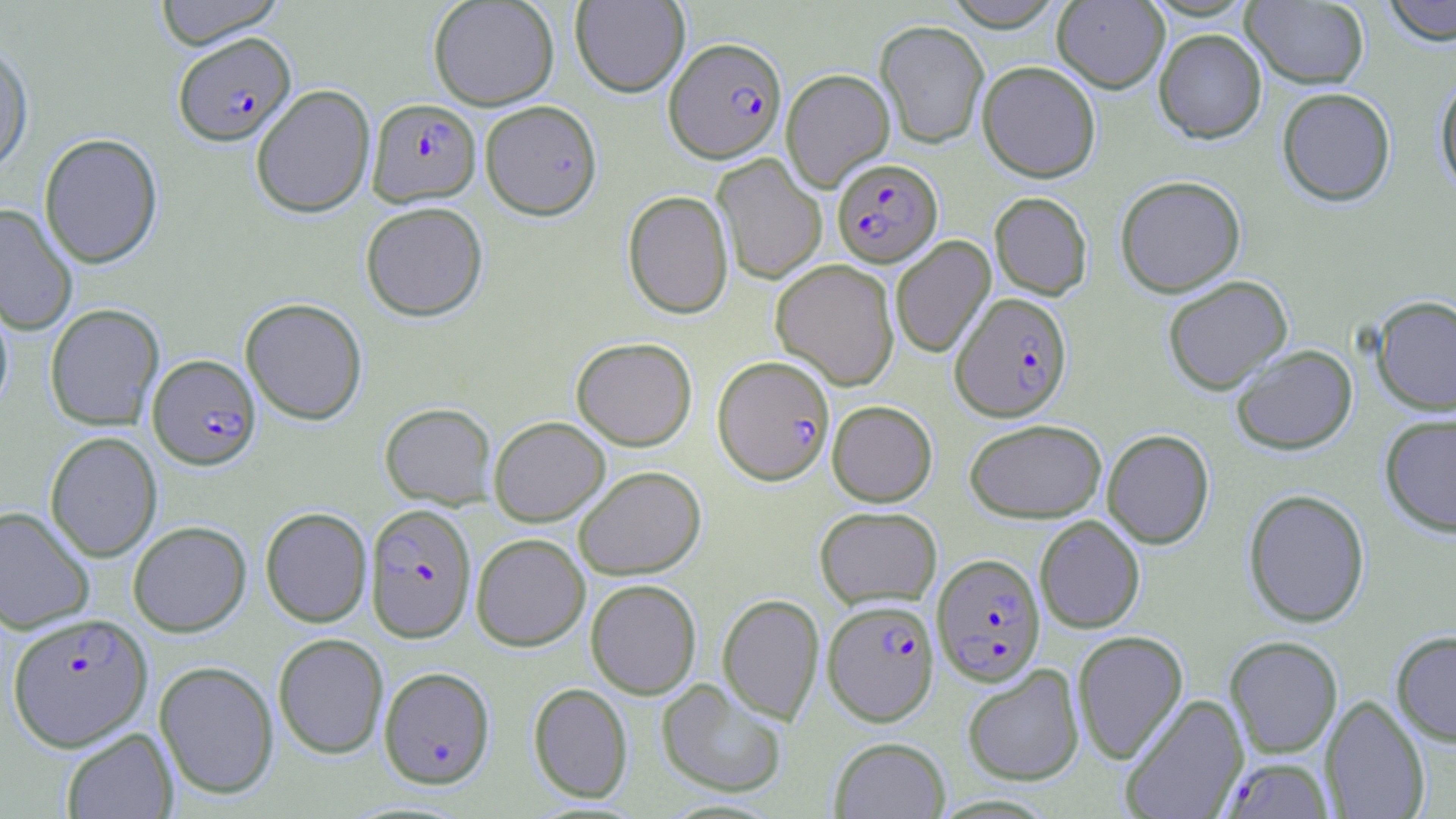
Summary:
  - Coordinate format: approximate bounding boxes as (x1,y1)-(x2,y2) corner pairs in pixels
  - Plasmodium falciparum-infected red blood cell locations: (173,32)-(296,146), (664,36)-(786,163), (368,99)-(481,206), (832,158)-(943,267), (951,292)-(1072,421), (147,354)-(261,470), (713,355)-(835,485), (364,503)-(477,642), (932,553)-(1046,686), (821,603)-(938,729), (6,612)-(153,751), (379,666)-(496,788), (1221,757)-(1334,818)
  - Uninfected red blood cell locations: (152,0)-(288,48), (428,0)-(559,110), (571,0)-(689,97), (943,0)-(1065,31), (1052,0)-(1169,93), (1241,0)-(1370,89), (1380,0)-(1456,45), (875,20)-(989,149), (1154,28)-(1267,143), (0,41)-(34,177), (977,60)-(1101,183), (781,68)-(895,191), (1434,76)-(1456,196), (250,84)-(376,218), (1277,87)-(1396,206), (479,100)-(602,220), (39,133)-(163,268), (712,154)-(827,286), (1115,175)-(1246,297), (623,190)-(733,319), (989,191)-(1093,300), (360,201)-(488,321), (0,203)-(78,336), (890,236)-(996,359), (771,259)-(899,390), (1162,275)-(1293,395), (0,295)-(14,416), (1371,295)-(1456,416), (240,298)-(368,424), (44,303)-(164,431), (571,337)-(697,450), (1230,344)-(1357,455), (827,400)-(937,506), (380,402)-(497,508), (1379,413)-(1456,537), (489,416)-(610,525), (964,419)-(1107,522), (1102,429)-(1214,549), (45,431)-(162,562), (573,466)-(706,580), (1243,488)-(1370,628), (0,505)-(95,634), (814,506)-(942,609), (260,507)-(372,627), (1035,516)-(1145,634), (128,521)-(251,636), (471,533)-(590,651), (585,579)-(702,699), (717,593)-(824,724), (1072,630)-(1188,764), (1391,630)-(1456,746), (273,633)-(389,758), (1225,636)-(1342,758), (154,661)-(279,799), (962,664)-(1084,786), (656,679)-(788,798), (528,682)-(633,803), (1120,694)-(1249,819), (1321,694)-(1430,819), (61,728)-(177,818), (829,736)-(950,818)
  - Slide-level diagnosis: Plasmodium falciparum
  - Image size: 1456×819 pixels
  - Modality: light microscopy
  - Magnification: 1000x
  - Preparation: thin blood smear
  - Stain: May-Grünwald-Giemsa
  - Field of view: one of a larger specimen